Rate the background quality.
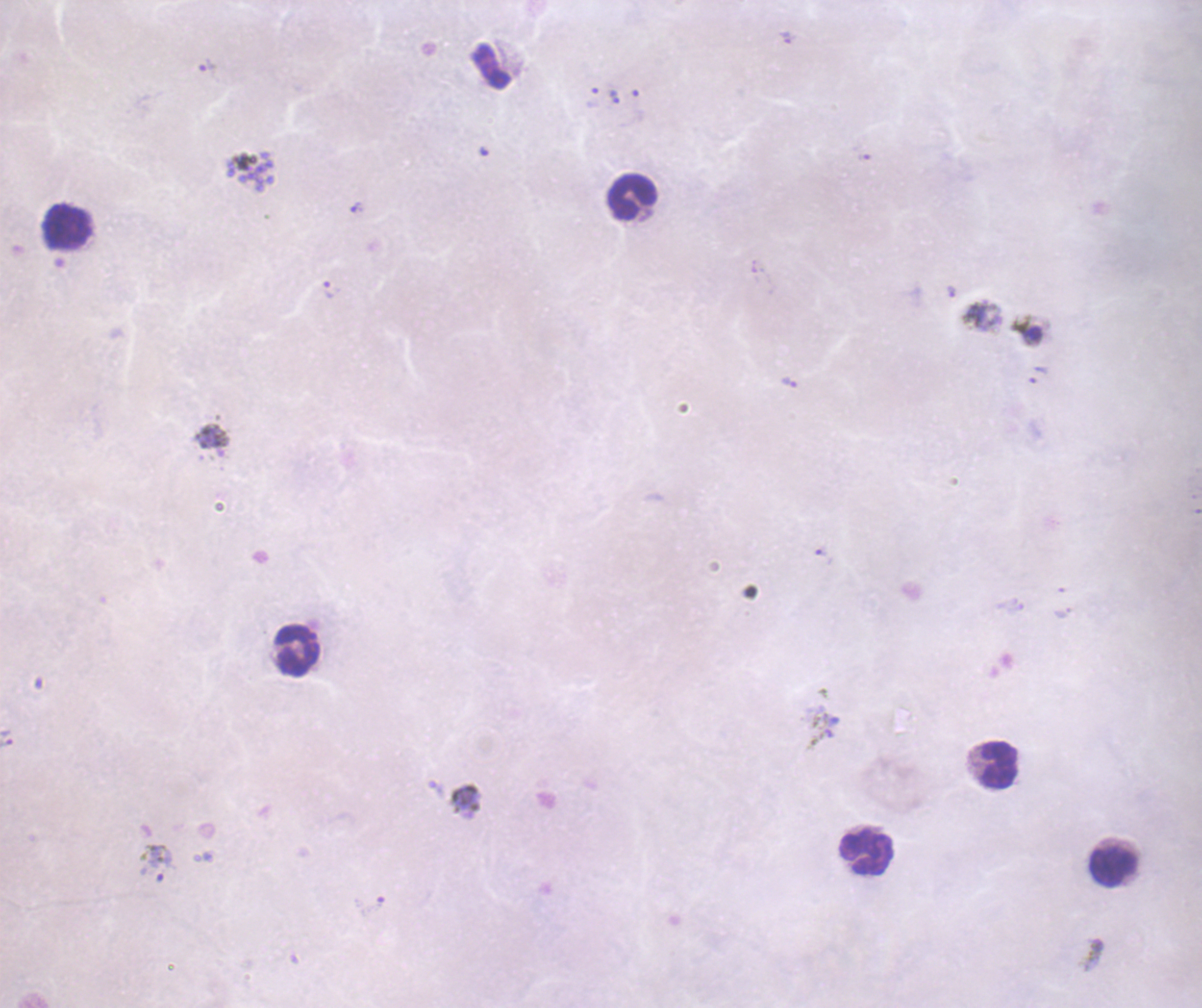
Unsatisfactory.

Approximate object centers, in pixels from the top-left corner. Trophozoite locations: (x=208, y=66), (x=614, y=97), (x=357, y=209), (x=331, y=290), (x=789, y=382), (x=821, y=552), (x=6, y=739), (x=158, y=863). Leukocyte locations: (x=632, y=198), (x=65, y=228), (x=298, y=651), (x=1000, y=766), (x=865, y=854), (x=1112, y=868). Coloration quality: bad. Result: malaria parasites identified. Thick smear of blood. Romanowsky stain. 100x magnification. Previously used in an actual diagnosis. One field from this slide. Image is 1202×1008 pixels.